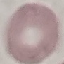
result: no malaria parasites detected
capture: smartphone through the microscope eyepiece
image_type: cell patch, automatically extracted from a larger field of view and resized to 64 × 64 pixels
preparation: thin blood smear
stain: Giemsa